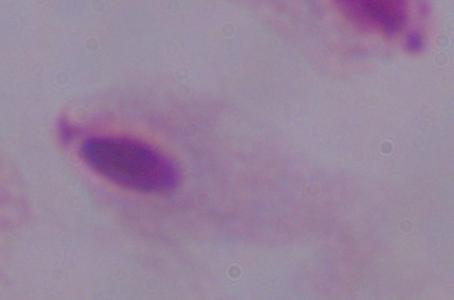
identification = trichomonad
magnification = 1000x
modality = micrograph